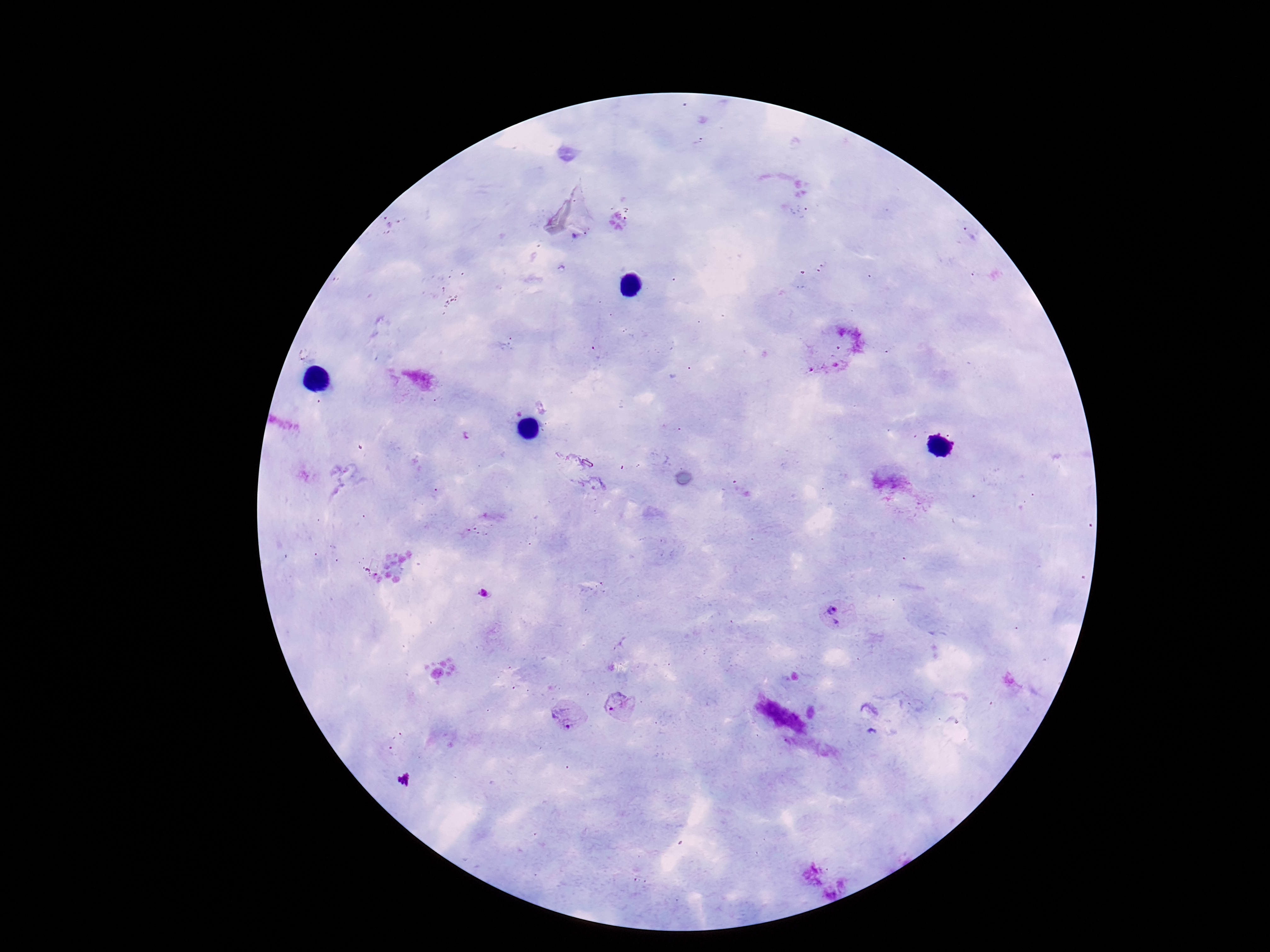 Approximate object centers, in pixels from the top-left corner. Plasmodium parasite locations: (x=483, y=593), (x=835, y=615), (x=622, y=706), (x=567, y=716), (x=404, y=780). Image is 1270×952 pixels. 100x magnification. Giemsa-stained preparation. Photographed through the microscope eyepiece with a smartphone camera. One field from this slide. Patient malaria status: positive. Thick peripheral-blood smear.